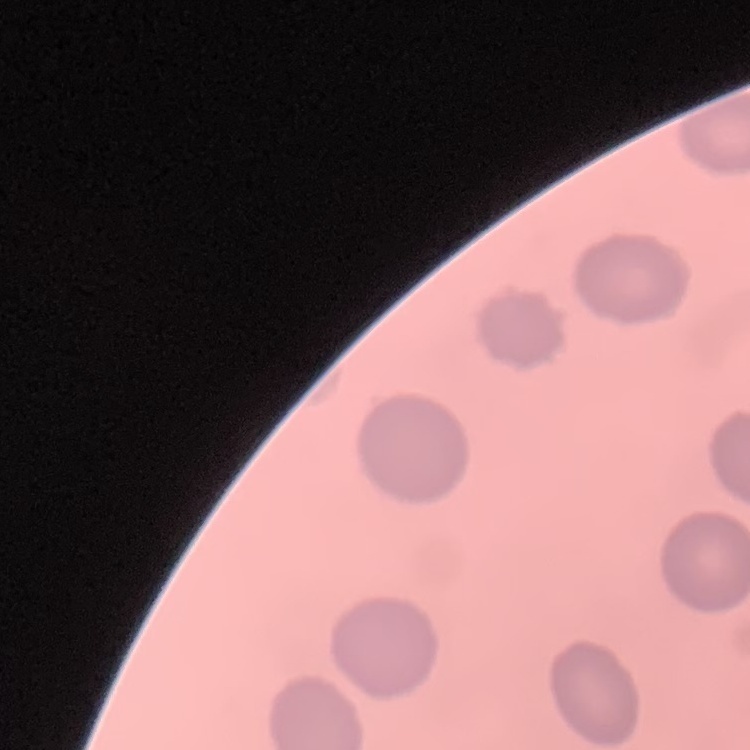

The red blood cells exhibit no rouleaux formation. Field's or Giemsa stain. Thin blood smear. One tile cut from a larger photomicrograph.